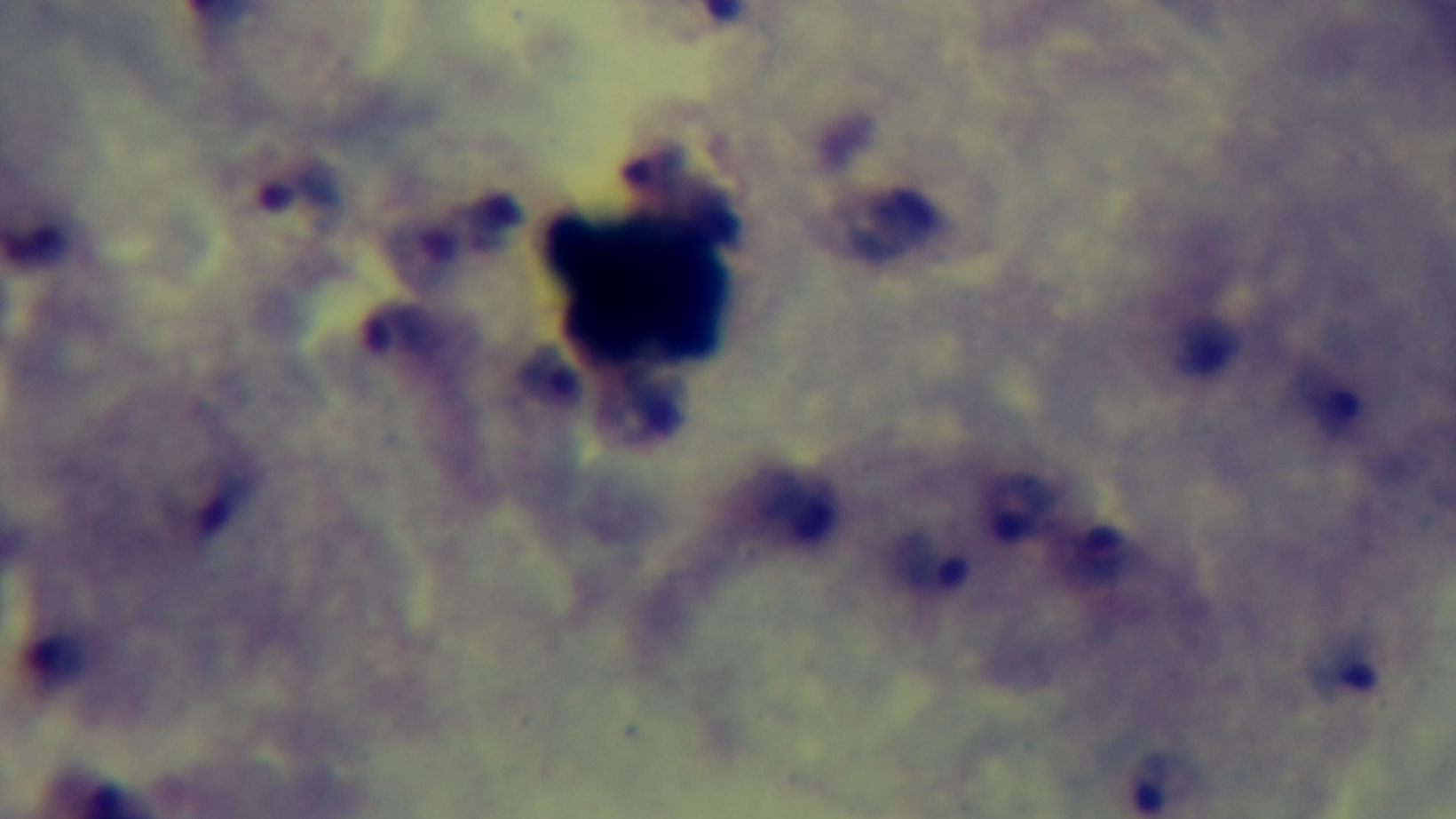
Summary:
  - Preparation: thick blood film
  - Capture: mounted 4K digital camera
  - Modality: light microscopy
  - Malaria status: infected
  - Objective: 100x oil immersion
  - Field of view: one from the slide
  - Stain: Giemsa